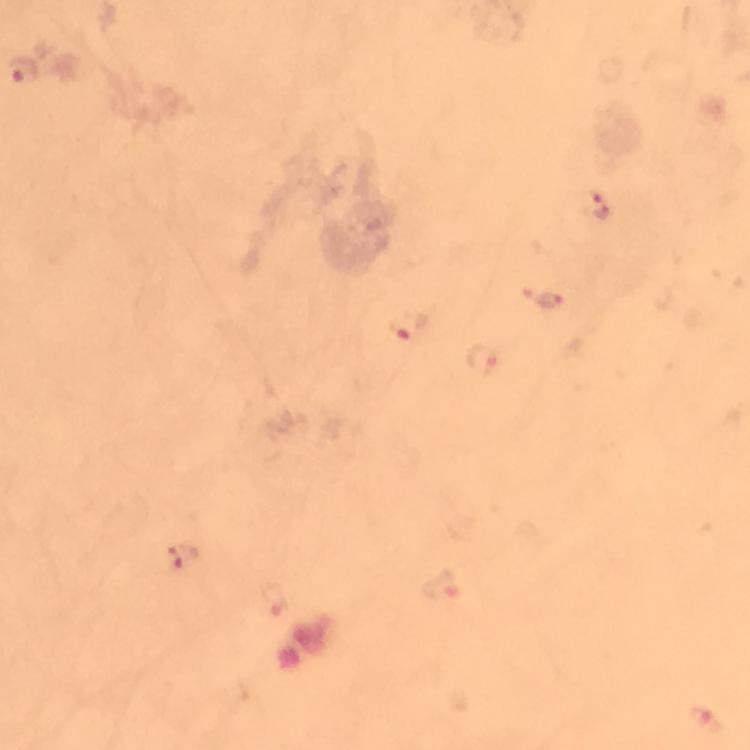

Approximate centers as (x, y) in pixels.
Summary:
  - Malaria parasite locations: (23, 70), (596, 205), (550, 301), (407, 327), (481, 361), (182, 555), (440, 583), (275, 600), (703, 720)
  - Capture: smartphone photograph through a microscope
  - Magnification: 100x
  - Image size: 750×750 pixels
  - Preparation: thick blood smear
  - Stain: Giemsa
  - Cropped from: a single field of view
  - Immersion oil: applied
  - Context: from a diagnostic examination for malaria